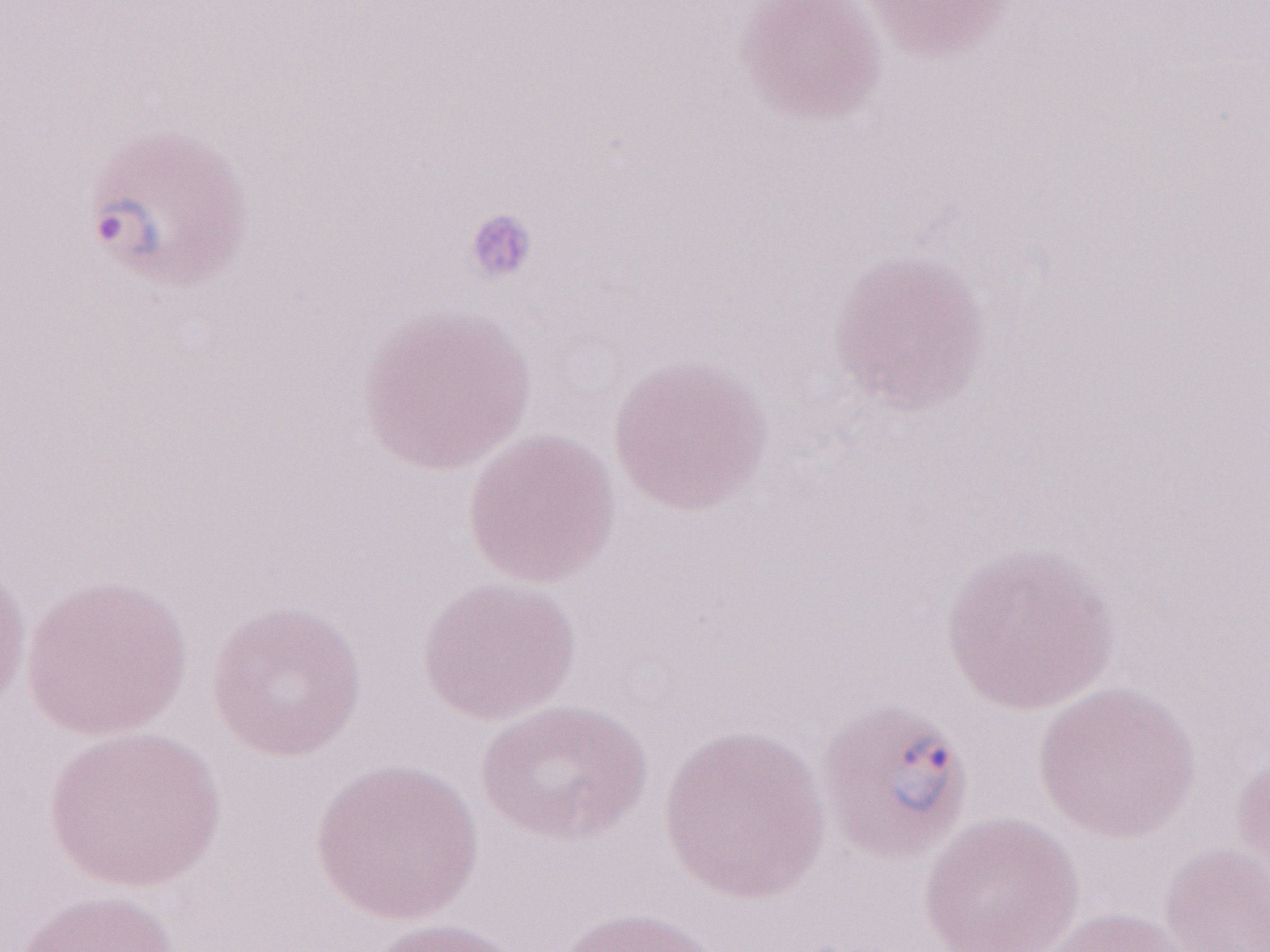
Thin blood film. One field of this slide. May-Grünwald-Giemsa-stained preparation. Image is 1270×952 pixels. Olympus BX43 microscope and DP73 digital camera. 1,000x magnification. Patient diagnosis: malaria infection.